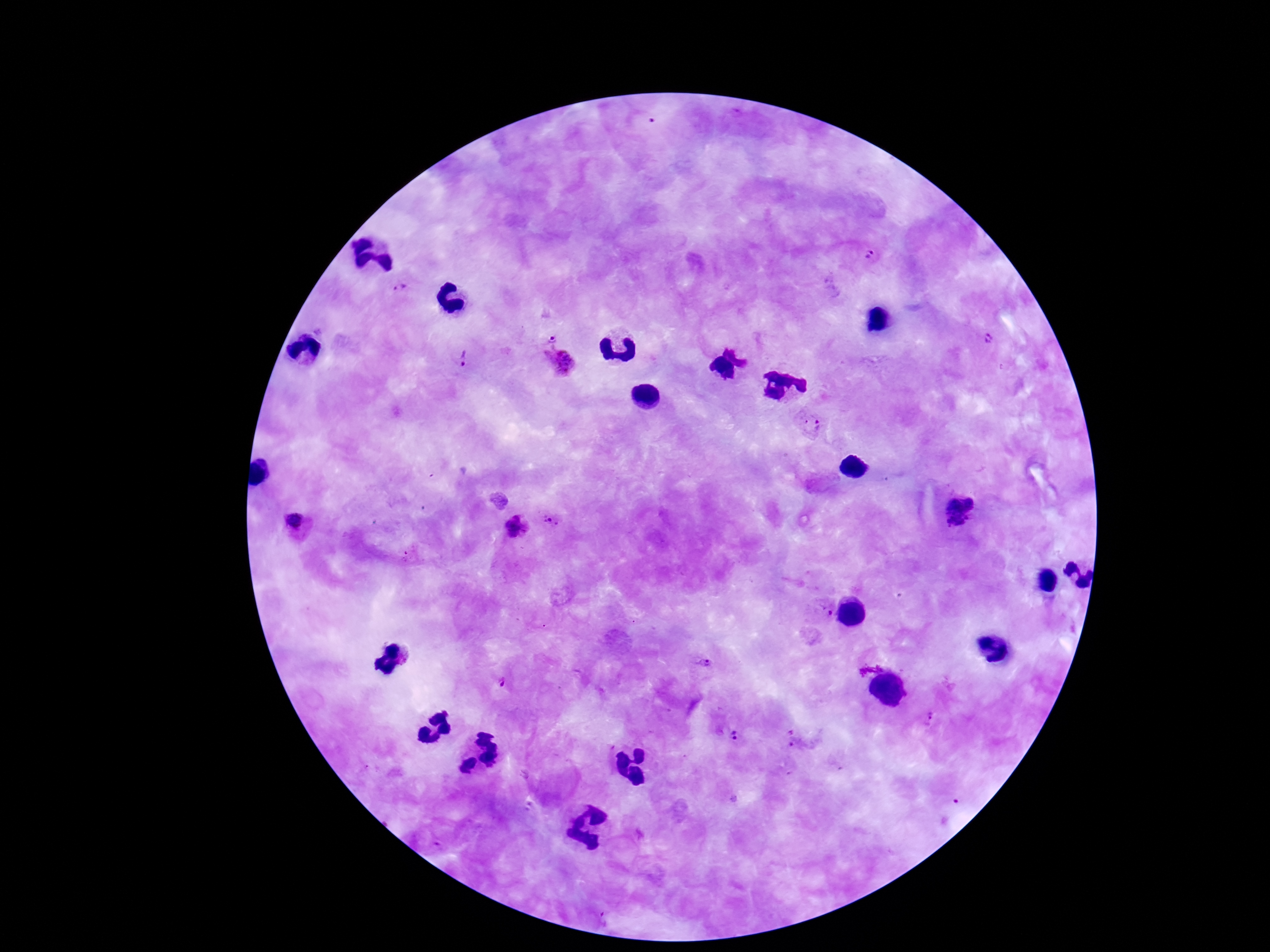
Approximate centers as (x, y) in pixels. Plasmodium parasite locations: (870, 258), (398, 287), (554, 335), (985, 337), (466, 358), (562, 367), (810, 423), (960, 509), (547, 519), (295, 525), (520, 527), (822, 613), (701, 666), (501, 685), (930, 717), (736, 736), (609, 915). Single field of view. Thick peripheral-blood smear. Smartphone photograph taken through the microscope eyepiece. Giemsa stain. Image is 1270×952 pixels. Patient malaria status: positive. 100x magnification.